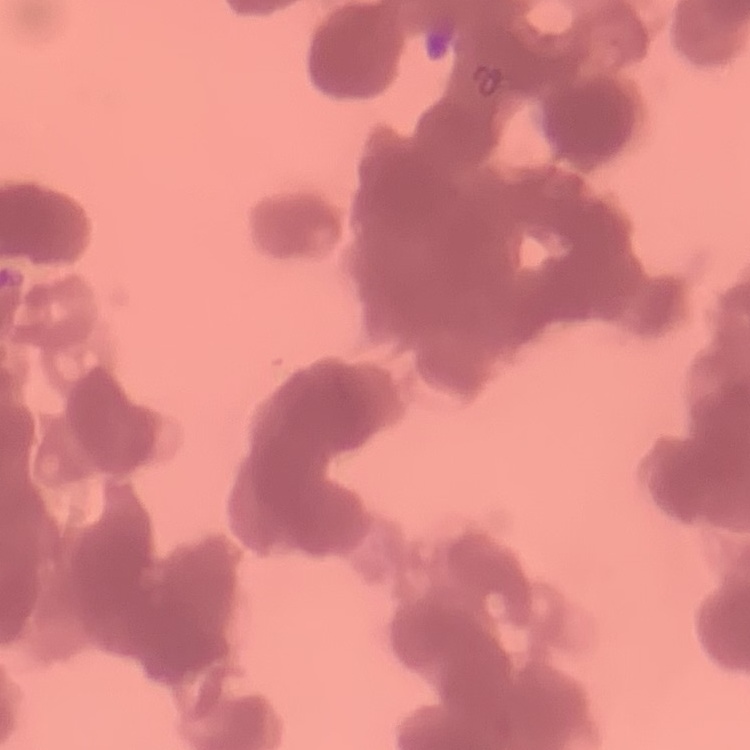

red blood cell morphology = rouleaux formation
stain = Field's or Giemsa
image type = one tile cut from a larger photomicrograph
preparation = thin peripheral smear